Identify the cell.
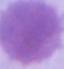
This is an erythrocyte.

Photomicrograph. Captured at 1000x magnification.